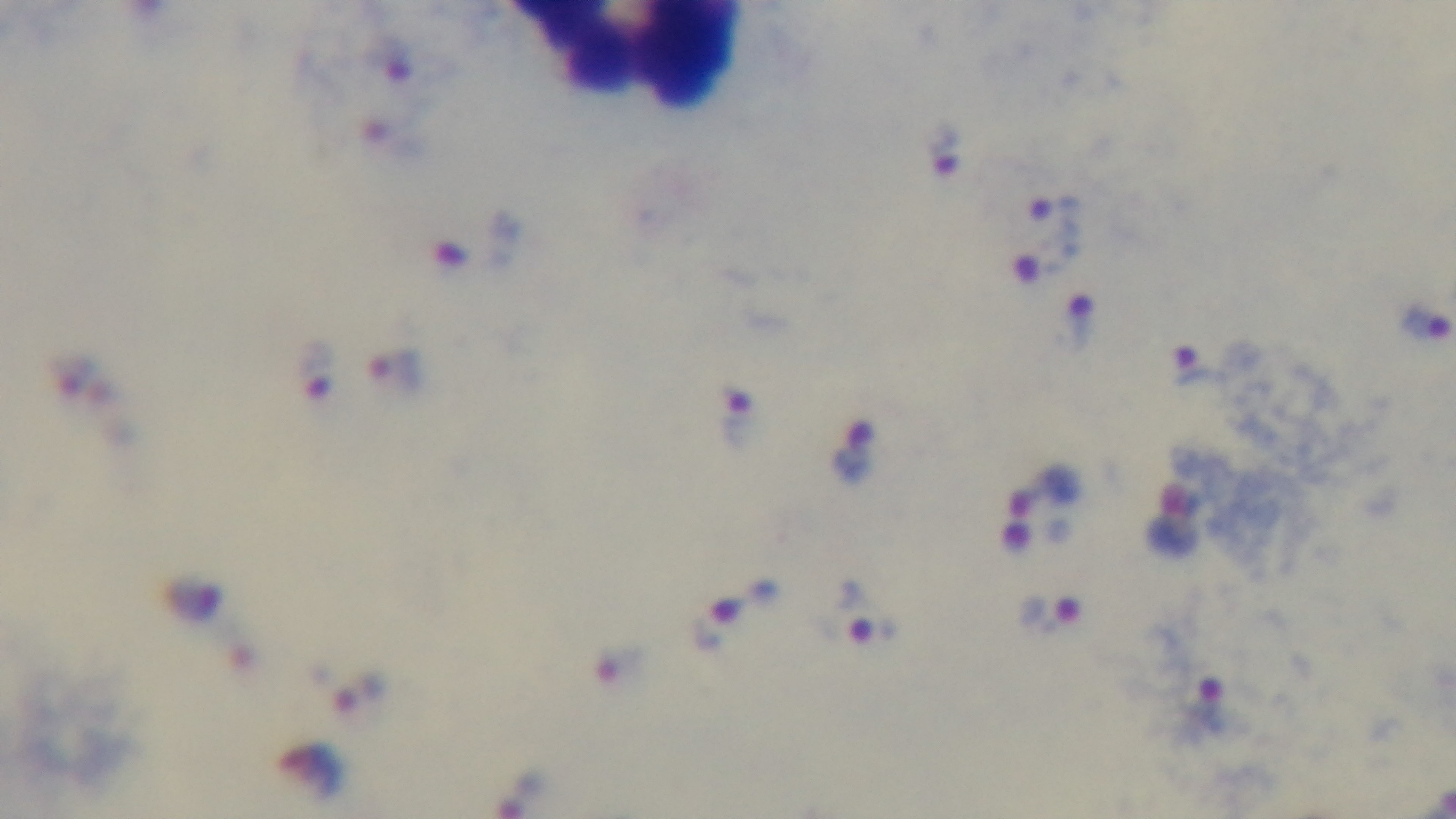

Summary:
  - Stain: Giemsa
  - Preparation: thick blood film
  - Objective: 100x oil immersion
  - Field of view: one from the slide
  - Malaria status: positive
  - Capture: mounted 4K digital camera
  - Modality: light microscopy